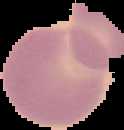

Summary:
  - Image size: 124×130 pixels
  - Image type: cell region segmented out of the field of view; surrounding area masked to black
  - Malaria status: uninfected
  - Preparation: thin blood smear